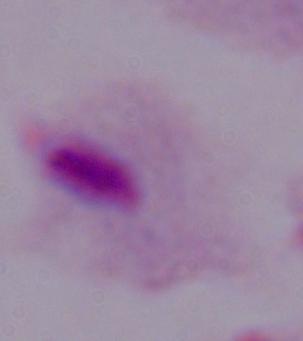
identification = trichomonad
modality = photomicrograph
magnification = 1000x